Report the malaria status of this cell.
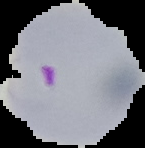
Parasitized.

Image is 145×148 pixels. From a thin blood film. Cell region segmented out of the field of view; the surrounding area is masked to black.